Locate every Plasmodium parasite.
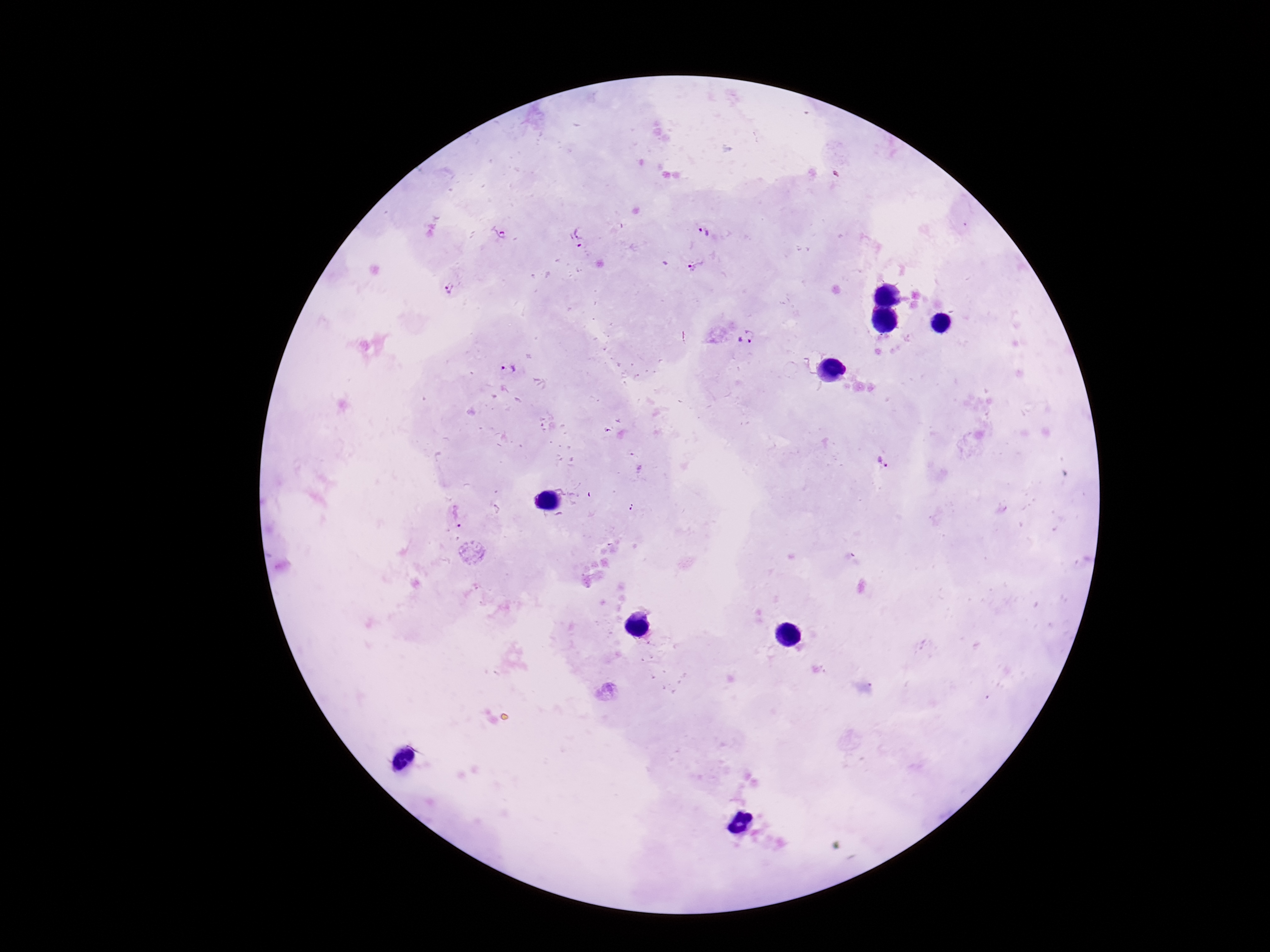

Approximate centers as (x, y) in pixels.
Plasmodium parasites: (704, 231), (581, 232), (500, 234), (572, 243), (697, 266), (449, 288), (748, 337), (508, 369), (884, 462), (630, 506), (456, 515).

One field from this slide. Thick blood smear. 100x magnification. Photographed through the microscope eyepiece with a smartphone camera. Image is 1270×952 pixels. Patient malaria status: infected. Giemsa stain.